Point out each Plasmodium parasite.
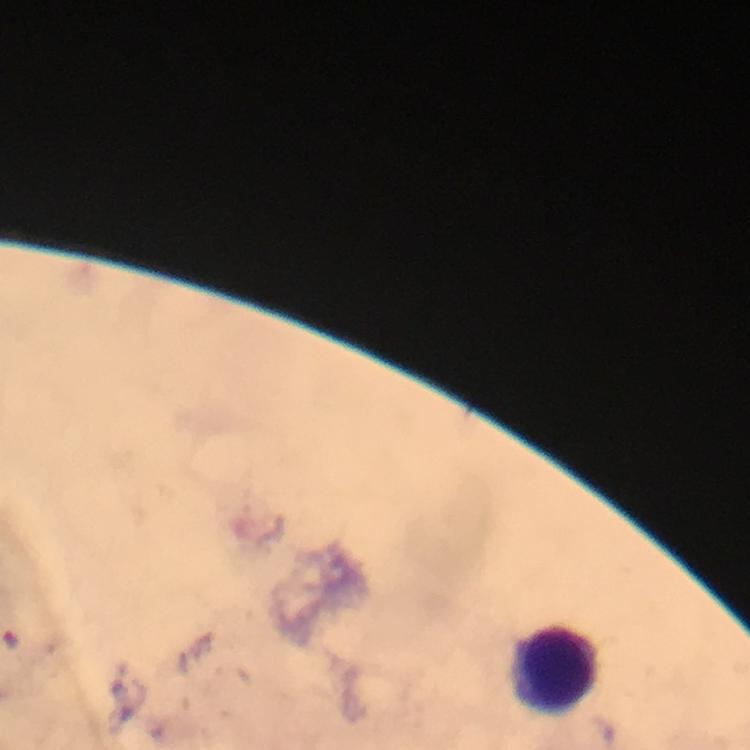
No Plasmodium parasites detected.

Approximate centers as {x, y} in pixels. Leukocyte locations: {553, 669}. At 100x magnification. Photographed through the microscope with a smartphone camera. Immersion oil applied. Giemsa-stained preparation. Image is 750×750 pixels. A crop from one field of view. From a malaria diagnostic workup. Thick blood smear.